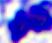

Summary:
  - Modality: photomicrograph
  - Identification: leukocyte
  - Magnification: 400x